Locate every Babesia divergens-infected red blood cell.
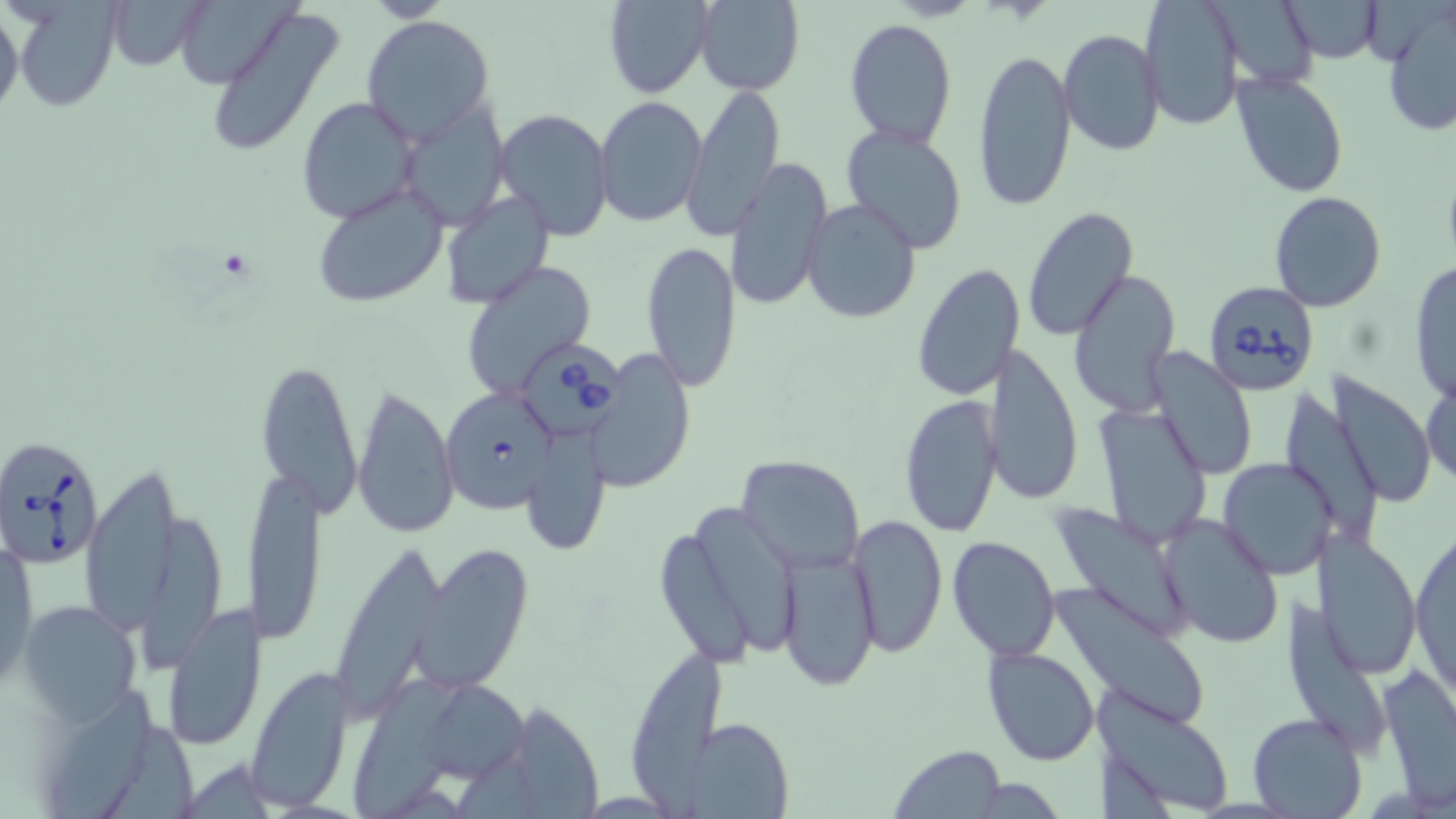

Approximate bounding boxes as (x1,y1)-(x2,y2) corner pairs in pixels.
Babesia divergens-infected red blood cells: (1203,282)-(1321,395), (519,345)-(630,437), (440,388)-(560,514), (0,433)-(103,570).

Summary:
  - Uninfected red blood cell locations: (105,0)-(209,70), (174,0)-(296,88), (603,0)-(715,100), (691,0)-(805,94), (1139,0)-(1244,129), (1283,0)-(1381,61), (0,1)-(23,127), (1207,1)-(1316,91), (10,5)-(120,114), (205,6)-(344,159), (1380,7)-(1456,137), (360,15)-(496,143), (845,18)-(956,149), (1058,29)-(1167,159), (973,47)-(1077,213), (1232,70)-(1348,197), (682,85)-(783,240), (594,95)-(707,228), (297,97)-(420,223), (400,103)-(509,230), (493,108)-(614,243), (840,122)-(969,254), (727,156)-(832,311), (310,182)-(449,307), (441,190)-(554,309), (1268,192)-(1389,313), (801,198)-(921,323), (1022,207)-(1139,342), (642,240)-(742,393), (457,259)-(599,399), (1408,259)-(1456,407), (912,264)-(1023,400), (1068,271)-(1181,420), (979,343)-(1082,506), (1152,349)-(1256,480), (587,350)-(697,491), (256,359)-(363,516), (1422,371)-(1455,492), (1332,375)-(1437,507), (351,382)-(460,540), (899,393)-(1004,539), (1094,402)-(1213,550), (522,434)-(612,555), (736,454)-(867,575), (1217,456)-(1333,581), (244,459)-(326,644), (80,460)-(185,638), (1044,503)-(1194,643), (699,509)-(798,655), (1157,512)-(1286,650), (845,514)-(947,657), (140,516)-(219,680), (1409,519)-(1455,700), (1313,529)-(1421,674), (947,536)-(1062,659), (656,537)-(755,668), (2,539)-(37,689), (410,543)-(533,695), (339,547)-(443,722), (775,550)-(879,689), (1054,581)-(1215,733), (161,601)-(269,750), (20,602)-(140,724), (982,646)-(1102,766), (636,651)-(728,819), (1378,661)-(1456,807), (246,664)-(353,812), (354,679)-(456,819), (436,680)-(534,786), (54,686)-(156,819), (1087,689)-(1232,817), (515,707)-(607,819), (1246,712)-(1367,819), (683,717)-(792,817), (105,721)-(198,819), (887,745)-(1008,819)
  - Slide-level diagnosis: Babesia divergens
  - Image size: 1456×819 pixels
  - Magnification: 1000x
  - Preparation: thin blood film
  - Modality: light microscopy
  - Field of view: single
  - Stain: May-Grünwald-Giemsa